Assess the morphology of the red blood cells.
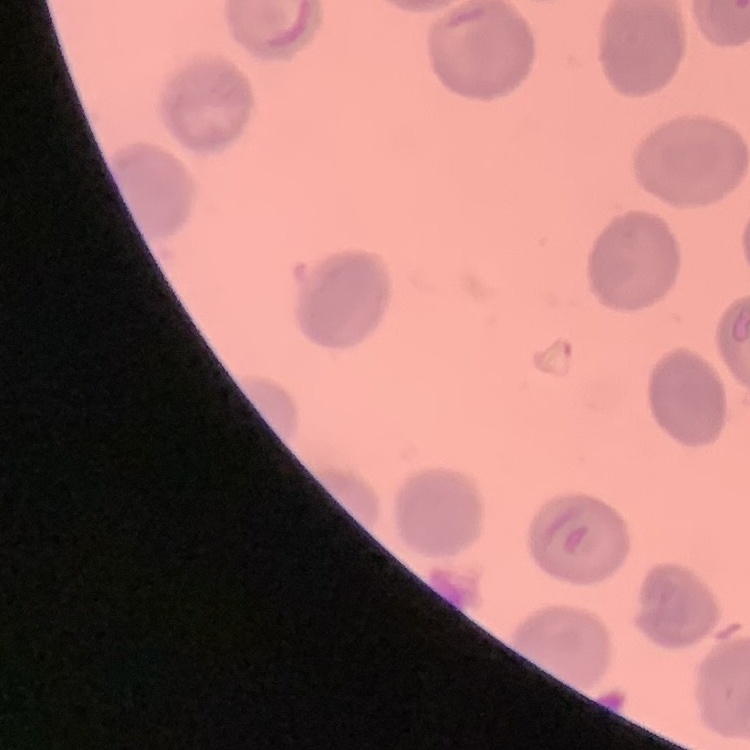
No rouleaux formation.

Square crop of a larger photomicrograph. Thin peripheral smear. Stained with either Field's or Giemsa.